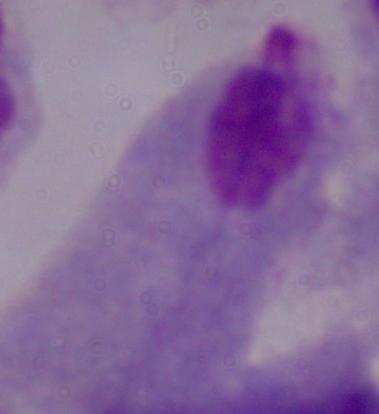
magnification = 1000x
modality = micrograph
identification = trichomonad